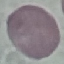

{
  "result": "no malaria parasites detected",
  "stain": "Giemsa",
  "image_type": "automatically extracted cell patch, resized to 64 × 64 pixels",
  "capture": "smartphone camera at the microscope eyepiece",
  "preparation": "thin blood film"
}